Assess this cell for malaria.
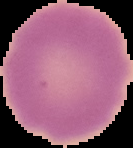
It is uninfected.

Image is 133×148 pixels. Cell region segmented out of the field of view; the surrounding area is masked to black. From a thin blood film.